Classify this cell by malaria status.
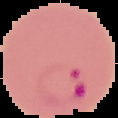

Parasitized.

image type = segmented cell region with the area outside set to black
image size = 118×118 pixels
preparation = thin blood film